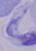

Summary:
  - Modality: micrograph
  - Magnification: 1000x
  - Identification: trypanosome